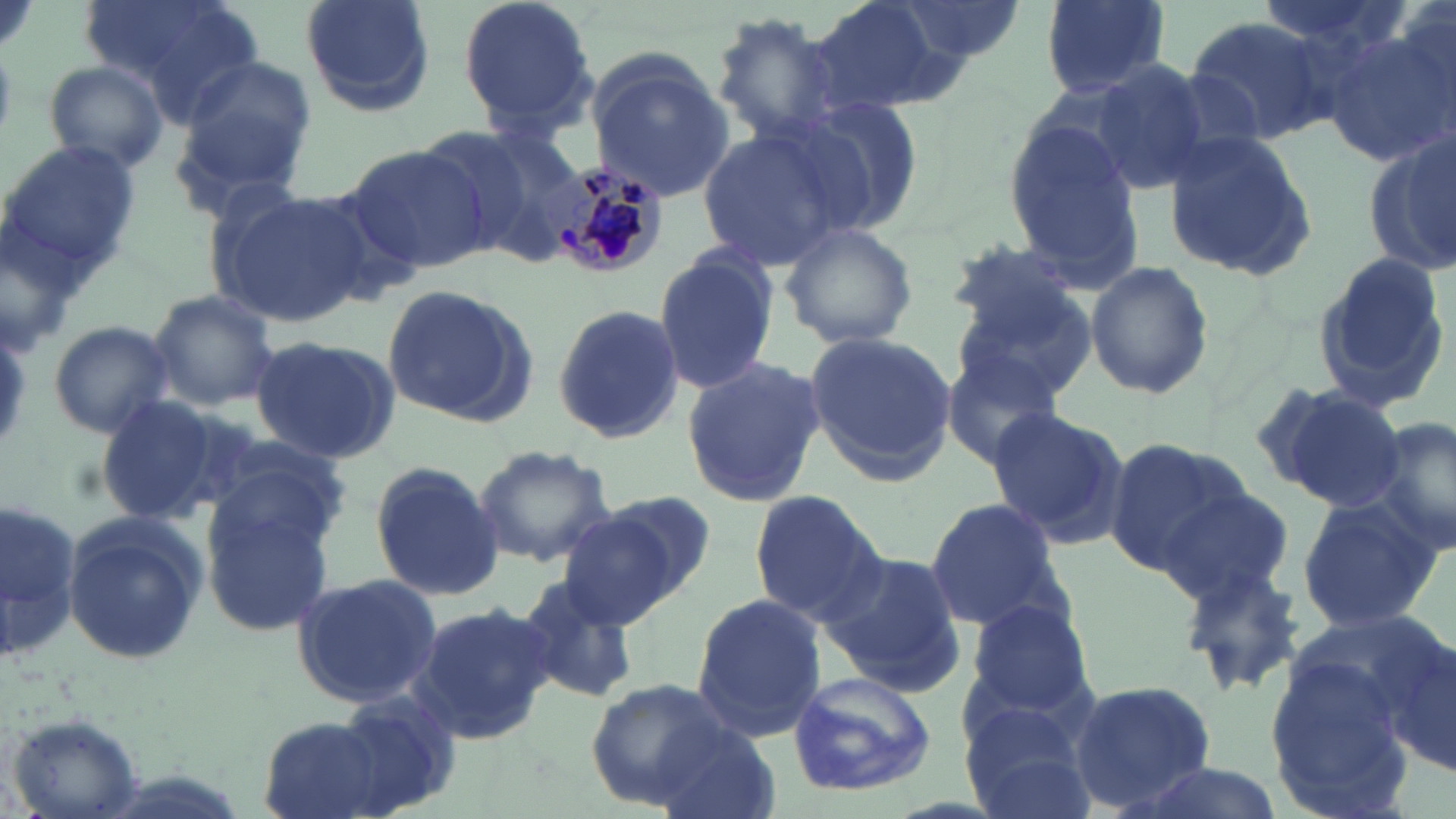
slide-level diagnosis = Plasmodium malariae
image size = 1456×819 pixels
Plasmodium malariae-infected red blood cell locations = approximate bounding boxes as [x1, y1, x2, y2] in pixels: [537, 158, 668, 282]
stain = May-Grünwald-Giemsa
modality = optical microscopy
uninfected red blood cell locations = approximate bounding boxes as [x1, y1, x2, y2] in pixels: [78, 0, 264, 114], [297, 0, 438, 120], [458, 0, 597, 138], [801, 0, 971, 118], [893, 0, 1026, 63], [1039, 0, 1170, 96], [1252, 0, 1413, 66], [709, 14, 846, 144], [1185, 14, 1338, 143], [1322, 23, 1456, 167], [586, 57, 736, 201], [41, 58, 171, 174], [175, 60, 317, 199], [1085, 61, 1214, 193], [791, 95, 929, 235], [1002, 112, 1142, 275], [697, 126, 848, 268], [1161, 129, 1318, 280], [462, 130, 589, 262], [1364, 132, 1456, 280], [4, 137, 142, 284], [343, 144, 493, 275], [207, 186, 370, 326], [778, 219, 919, 353], [941, 240, 1087, 345], [656, 245, 781, 394], [1312, 247, 1452, 411], [1084, 260, 1215, 400], [381, 283, 537, 427], [954, 287, 1098, 403], [147, 289, 281, 410], [550, 303, 684, 446], [45, 319, 175, 439], [801, 331, 958, 485], [250, 336, 400, 464], [941, 352, 1068, 469], [680, 358, 827, 509], [1272, 385, 1407, 511], [95, 392, 240, 528], [984, 407, 1126, 549], [1370, 417, 1456, 559], [205, 436, 354, 548], [1102, 438, 1248, 577], [472, 445, 616, 568], [368, 460, 504, 600], [1154, 488, 1298, 605], [602, 489, 718, 601], [747, 489, 888, 623], [197, 491, 338, 635], [1296, 492, 1441, 636], [0, 496, 86, 667], [921, 496, 1065, 632], [63, 509, 205, 665], [557, 510, 685, 630], [823, 550, 965, 694], [1177, 557, 1307, 698], [292, 572, 443, 710], [512, 573, 637, 704], [692, 594, 829, 739], [963, 596, 1094, 716], [409, 600, 557, 746], [1378, 632, 1456, 778], [1264, 656, 1411, 803], [785, 671, 938, 798], [582, 679, 735, 805], [1070, 680, 1219, 813], [326, 686, 464, 817], [960, 709, 1097, 819], [6, 716, 147, 819], [259, 716, 383, 817], [648, 719, 783, 819], [1125, 761, 1289, 819]
magnification = 1000x
preparation = thin blood film
field of view = single